State which cell type is depicted.
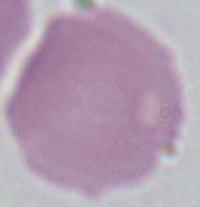

An erythrocyte.

Micrograph. 1000x magnification.